Locate every malaria parasite.
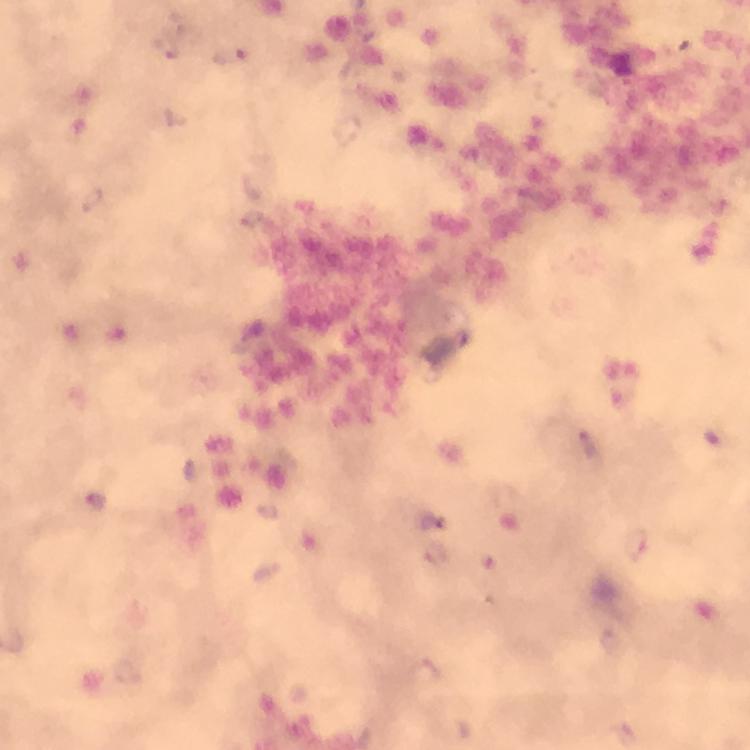
Approximate centers as {x, y} in pixels.
Malaria parasites: {164, 46}, {230, 55}, {589, 445}, {636, 544}, {438, 554}, {426, 672}.

From a diagnostic examination for malaria. Giemsa stain. Cropped region of a single field of view. At 100x magnification. Thick blood film. Immersion oil was used. Photographed with a smartphone mounted on the microscope. Image is 750×750 pixels.